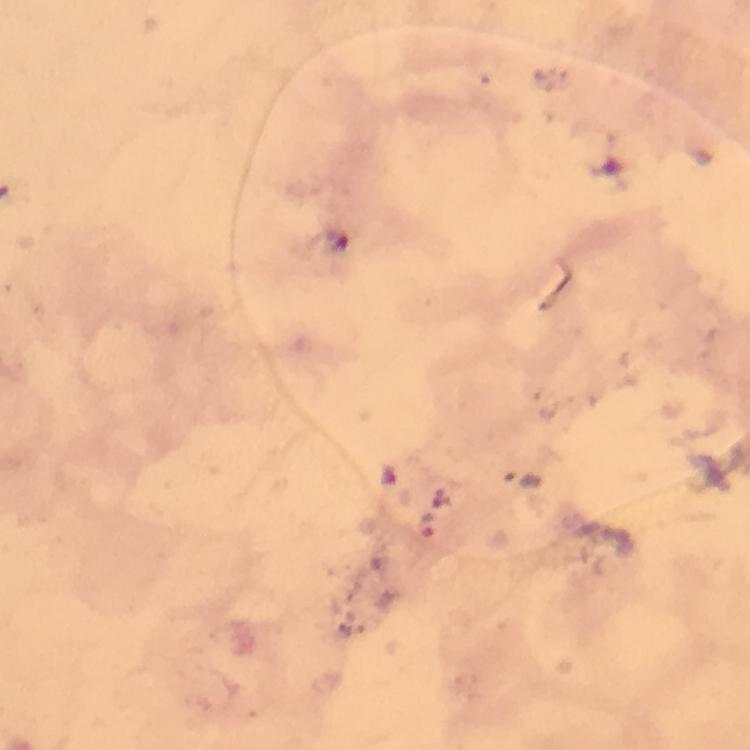 Approximate object centers, in pixels from the top-left corner. Malaria parasite locations: (x=426, y=526). Cropped region of a single field of view. 100x magnification. From a diagnostic examination for malaria. Thick blood smear. Image is 750×750 pixels. Immersion oil was used. Smartphone photograph taken through a microscope. Giemsa-stained preparation.